Point out each Plasmodium parasite.
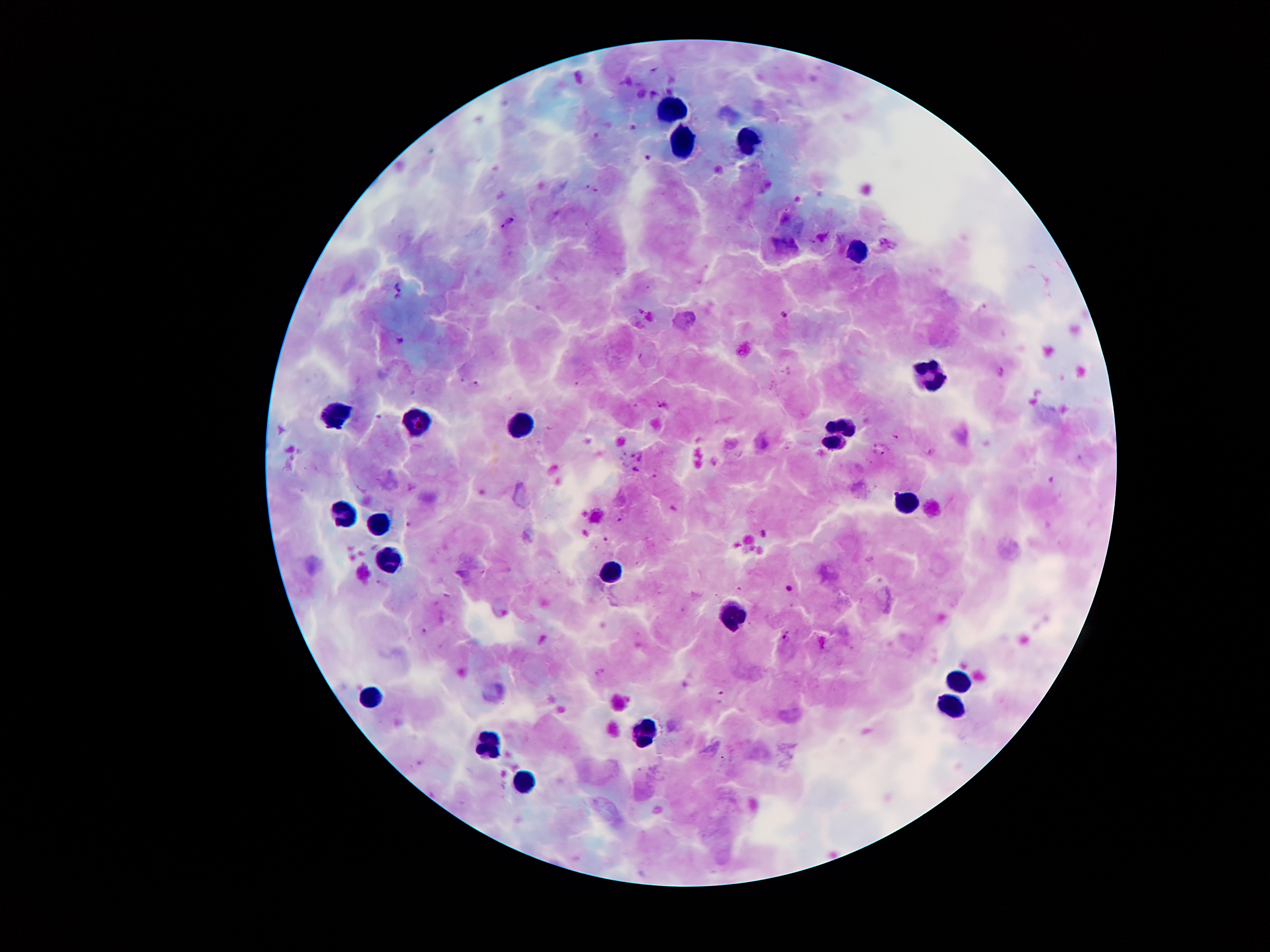

Approximate centers as {x, y} in pixels.
Plasmodium parasites: {647, 157}, {587, 186}, {596, 191}, {512, 218}, {503, 226}, {399, 287}, {785, 314}, {399, 342}, {477, 385}, {663, 406}, {879, 453}, {640, 456}, {633, 469}, {414, 486}, {619, 520}, {408, 523}, {606, 538}, {789, 589}, {787, 638}, {599, 672}, {719, 696}.

Summary:
  - Leukocyte locations: {675, 111}, {681, 141}, {746, 143}, {860, 251}, {931, 376}, {334, 414}, {415, 424}, {523, 430}, {842, 431}, {903, 503}, {343, 517}, {377, 523}, {390, 561}, {613, 572}, {728, 617}, {960, 683}, {374, 700}, {948, 701}, {640, 731}, {490, 738}, {520, 785}
  - Capture: smartphone camera through the microscope eyepiece
  - Magnification: 100x
  - Stain: Giemsa
  - Preparation: thick blood film
  - Field of view: one from this slide
  - Patient malaria status: positive for Plasmodium falciparum
  - Image size: 1270×952 pixels